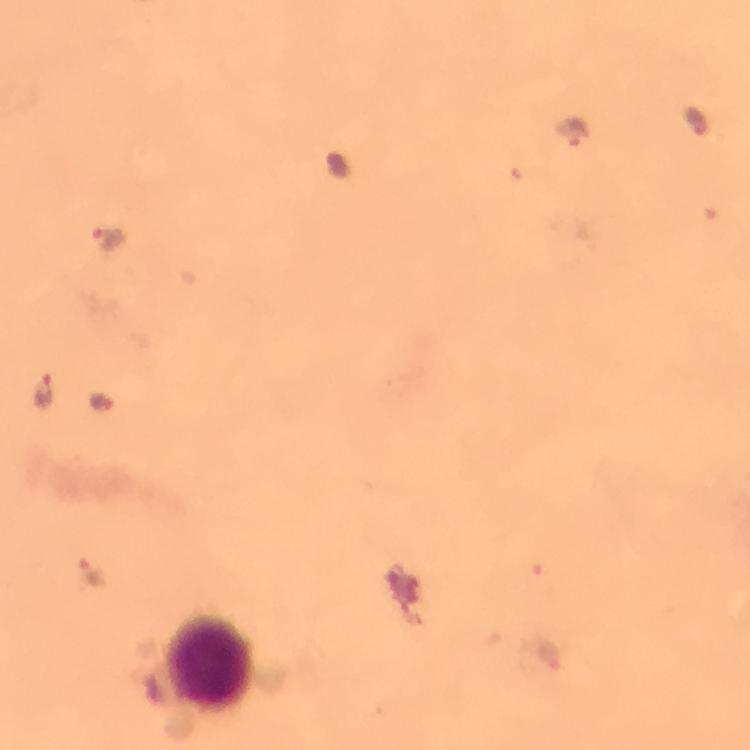
capture = smartphone mounted on the microscope
preparation = thick smear
stain = Giemsa
cropped from = a single field of view
immersion oil = used
Plasmodium parasite locations = approximate centers as (x, y) in pixels: (697, 119), (574, 135), (110, 242), (43, 391), (102, 404), (92, 572), (546, 654)
context = from a diagnostic examination for malaria
magnification = 100x
leukocyte locations = approximate centers as (x, y) in pixels: (215, 665)
image size = 750×750 pixels